State the blood parasite species.
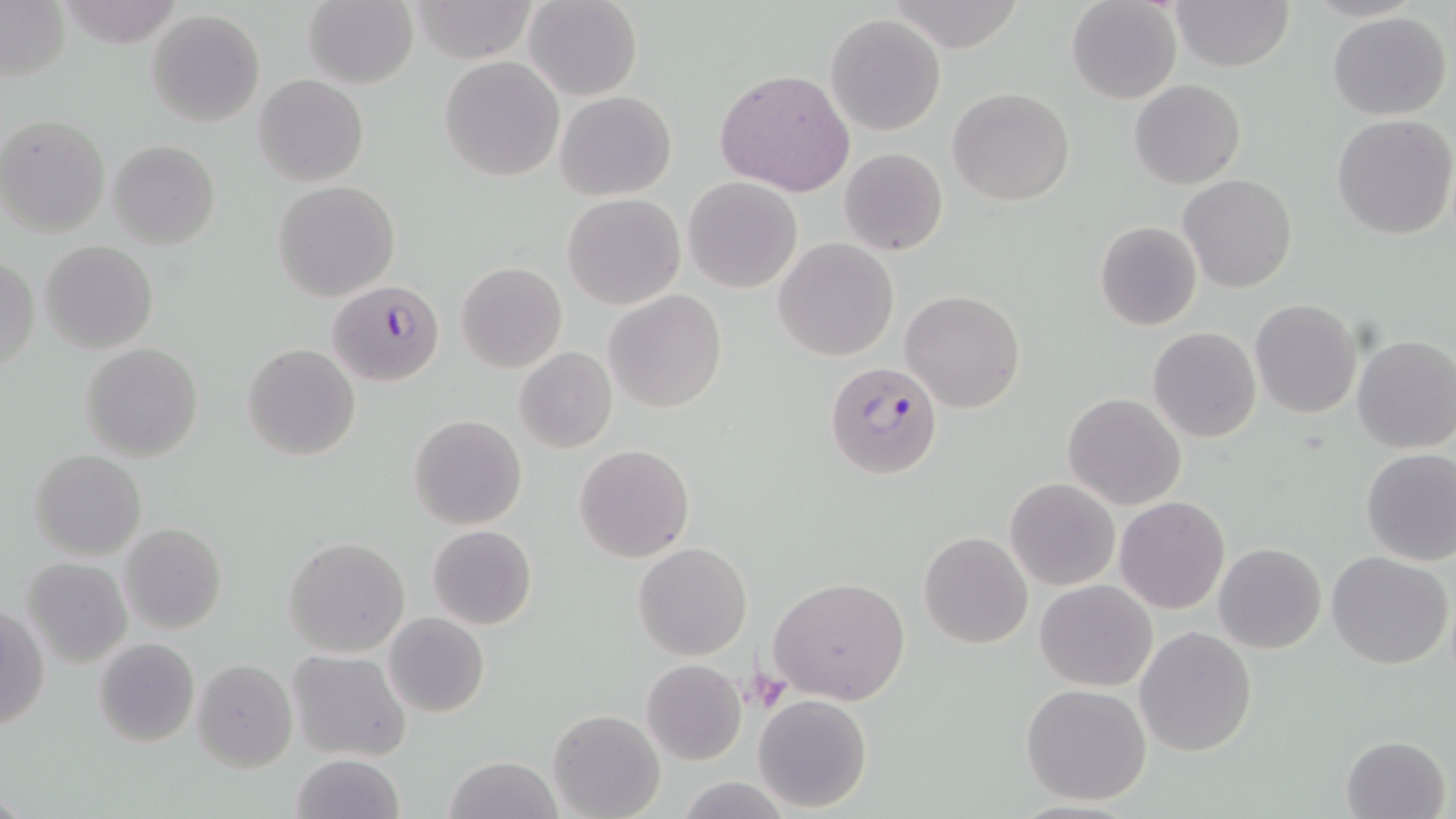

Plasmodium falciparum.

field of view = single
stain = May-Grünwald-Giemsa
Plasmodium falciparum-infected red blood cell locations = approximate bounding boxes as [x1, y1, x2, y2] in pixels: [323, 277, 449, 390], [824, 361, 942, 481]
uninfected red blood cell locations = approximate bounding boxes as [x1, y1, x2, y2] in pixels: [58, 0, 187, 48], [303, 0, 418, 89], [409, 0, 539, 63], [525, 0, 642, 101], [1066, 0, 1183, 104], [1169, 0, 1294, 72], [0, 2, 69, 83], [147, 10, 266, 127], [1327, 11, 1452, 120], [826, 13, 945, 136], [439, 56, 566, 182], [715, 67, 857, 197], [253, 74, 369, 187], [1129, 79, 1245, 189], [948, 87, 1075, 205], [555, 90, 675, 200], [0, 113, 109, 237], [1331, 115, 1456, 240], [107, 139, 221, 249], [839, 147, 949, 257], [1180, 174, 1297, 293], [683, 176, 802, 293], [272, 181, 400, 302], [561, 193, 685, 310], [1094, 221, 1203, 332], [775, 237, 900, 362], [42, 240, 158, 354], [1, 254, 39, 374], [455, 262, 567, 373], [902, 289, 1025, 412], [604, 290, 726, 412], [1250, 299, 1362, 419], [1148, 327, 1261, 444], [1351, 335, 1456, 453], [242, 342, 360, 460], [79, 343, 204, 462], [515, 347, 618, 454], [1063, 392, 1185, 510], [408, 414, 527, 531], [573, 444, 695, 563], [1358, 447, 1456, 565], [29, 449, 146, 561], [1006, 478, 1120, 590], [1115, 496, 1231, 614], [119, 522, 226, 634], [427, 525, 537, 630], [919, 531, 1033, 648], [283, 535, 409, 657], [633, 542, 751, 661], [1213, 542, 1326, 655], [1327, 552, 1454, 671], [21, 557, 133, 668], [768, 575, 911, 705], [1035, 579, 1158, 691], [1, 605, 48, 734], [385, 613, 489, 716], [1135, 625, 1257, 758], [94, 637, 200, 749], [287, 649, 412, 761], [192, 658, 296, 772], [641, 658, 747, 767], [1021, 682, 1153, 806], [752, 694, 872, 811], [548, 709, 665, 818], [1341, 734, 1451, 819], [290, 753, 406, 819], [444, 755, 564, 818]
magnification = 1000x
preparation = thin blood smear
platelet locations = approximate bounding boxes as [x1, y1, x2, y2] in pixels: [749, 666, 790, 710]
image size = 1456×819 pixels
modality = optical microscopy